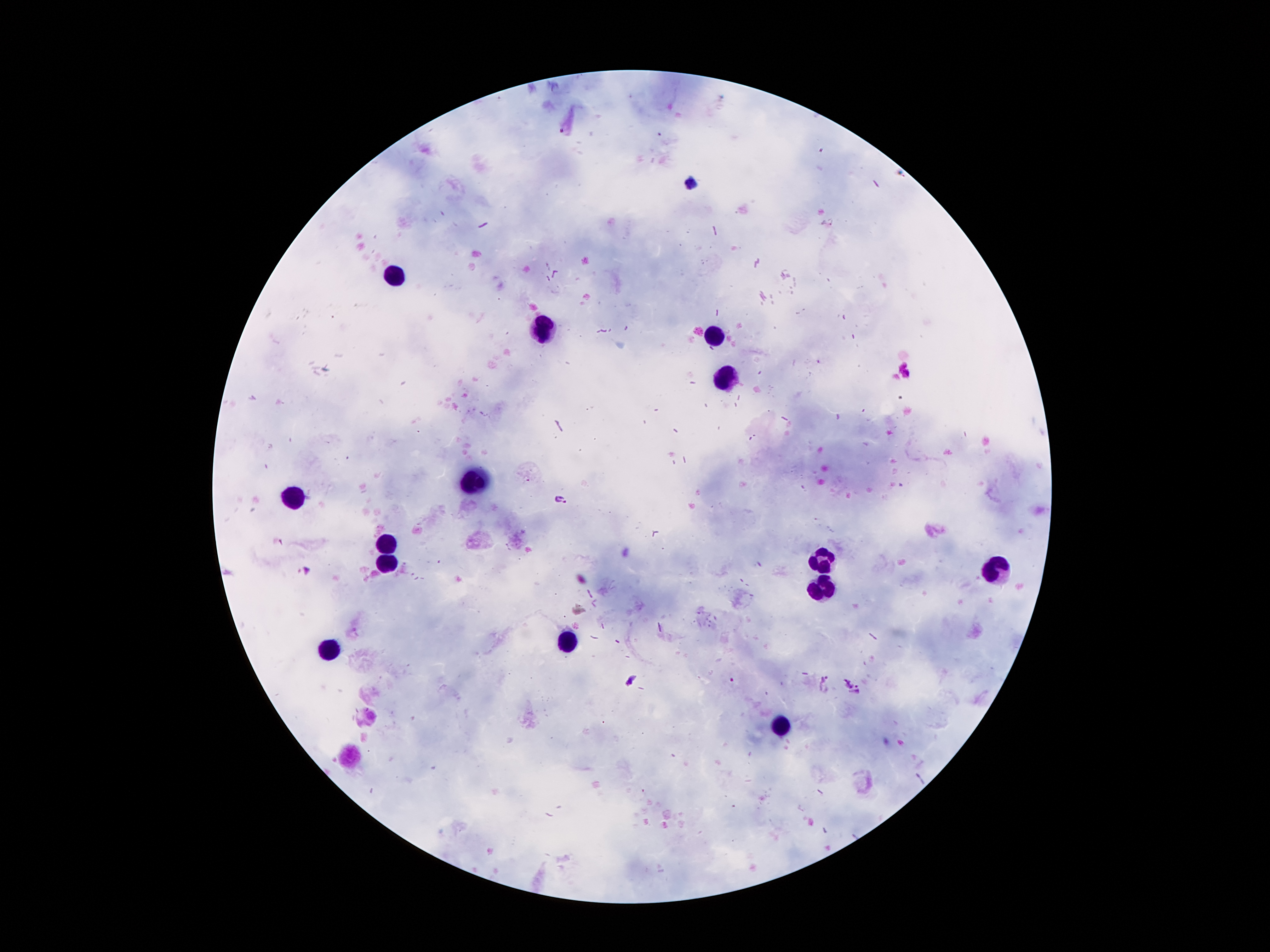 Approximate centers as {x, y} in pixels. Leukocyte locations: {397, 275}, {547, 329}, {714, 335}, {724, 377}, {475, 479}, {292, 499}, {391, 544}, {823, 560}, {390, 563}, {1000, 566}, {822, 587}, {567, 643}, {333, 650}, {781, 727}. Malaria parasite locations: {561, 499}, {305, 572}, {630, 679}, {858, 692}. Thick blood smear. One field from this slide. Image is 1270×952 pixels. Photographed through the microscope eyepiece with a smartphone camera. Patient malaria status: positive for Plasmodium falciparum. Giemsa stain. 100x magnification.